Assess the morphology of the erythrocytes.
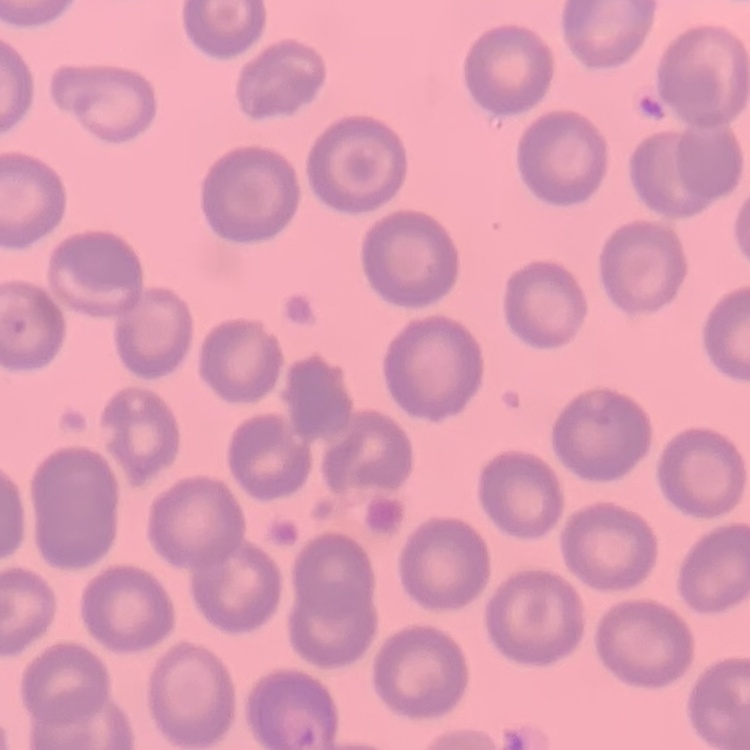
They show no rouleaux formation.

image type = square crop of a larger photomicrograph
preparation = thin blood smear
stain = Field's or Giemsa